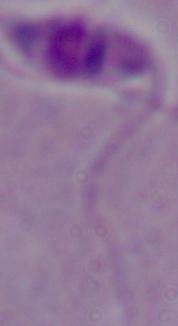
magnification = 1000x
modality = micrograph
identification = Leishmania